Report the malaria status of this cell.
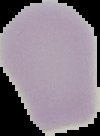

It is uninfected.

Image is 100×136 pixels. The area outside the segmented cell region is set to black. From a thin blood film.